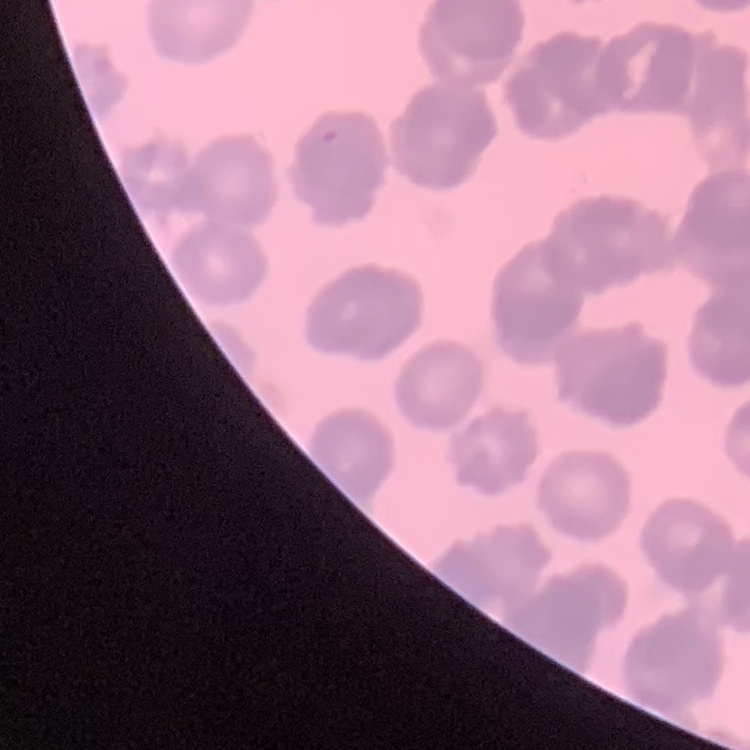

{
  "red_blood_cell_morphology": "rouleaux formation",
  "preparation": "thin blood film",
  "image_type": "one tile cut from a larger photomicrograph",
  "stain": "Field's or Giemsa"
}